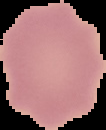

Malaria status: uninfected. Cell region segmented out of the field of view; the surrounding area is masked to black. Image is 106×130 pixels. From a thin blood film.